Comment on the morphology of the red blood cells.
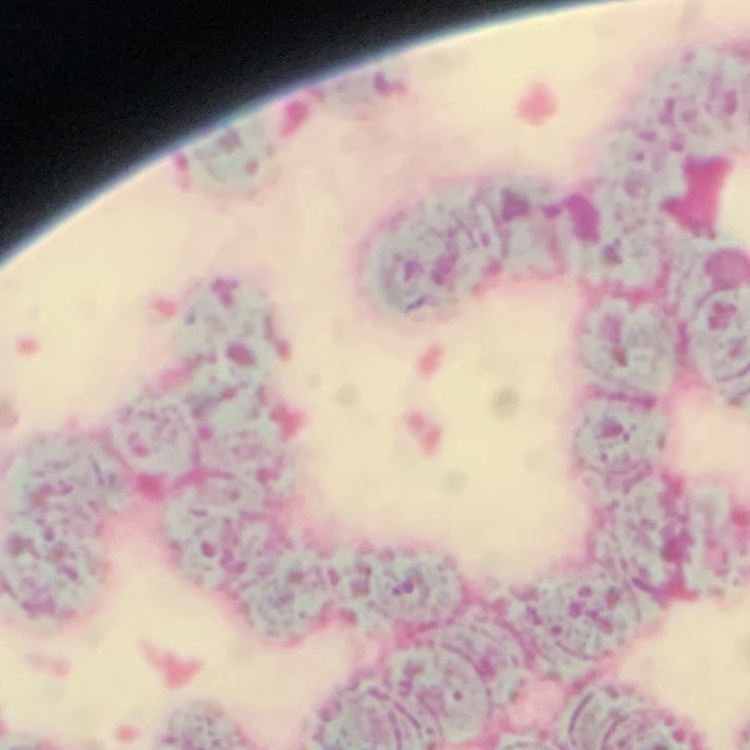
They show rouleaux formation.

Summary:
  - Preparation: thin peripheral smear
  - Stain: Field's or Giemsa
  - Image type: one tile cut from a larger photomicrograph